Assess the morphology of the erythrocytes.
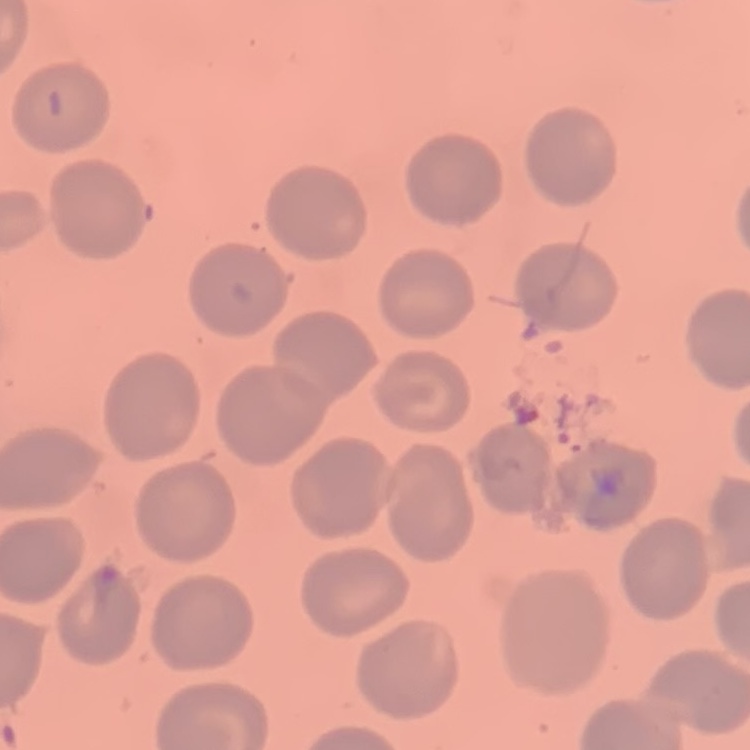
No rouleaux formation.

preparation = thin blood smear
image type = one tile cut from a larger photomicrograph
stain = Field's or Giemsa